Locate every malaria parasite.
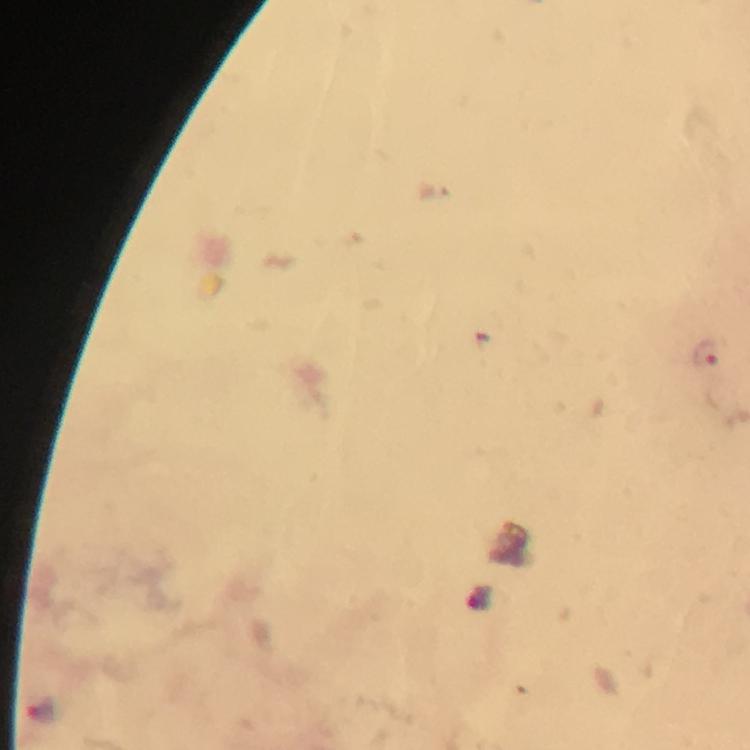
Approximate object centers, in pixels from the top-left corner.
Malaria parasites: (x=706, y=352).

magnification = 100x
context = from a malaria diagnostic workup
image size = 750×750 pixels
capture = smartphone photograph through a microscope
preparation = thick smear
cropped from = one field of view
immersion oil = used
stain = Giemsa